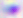

400x magnification. Toxoplasma gondii is shown. Photomicrograph.